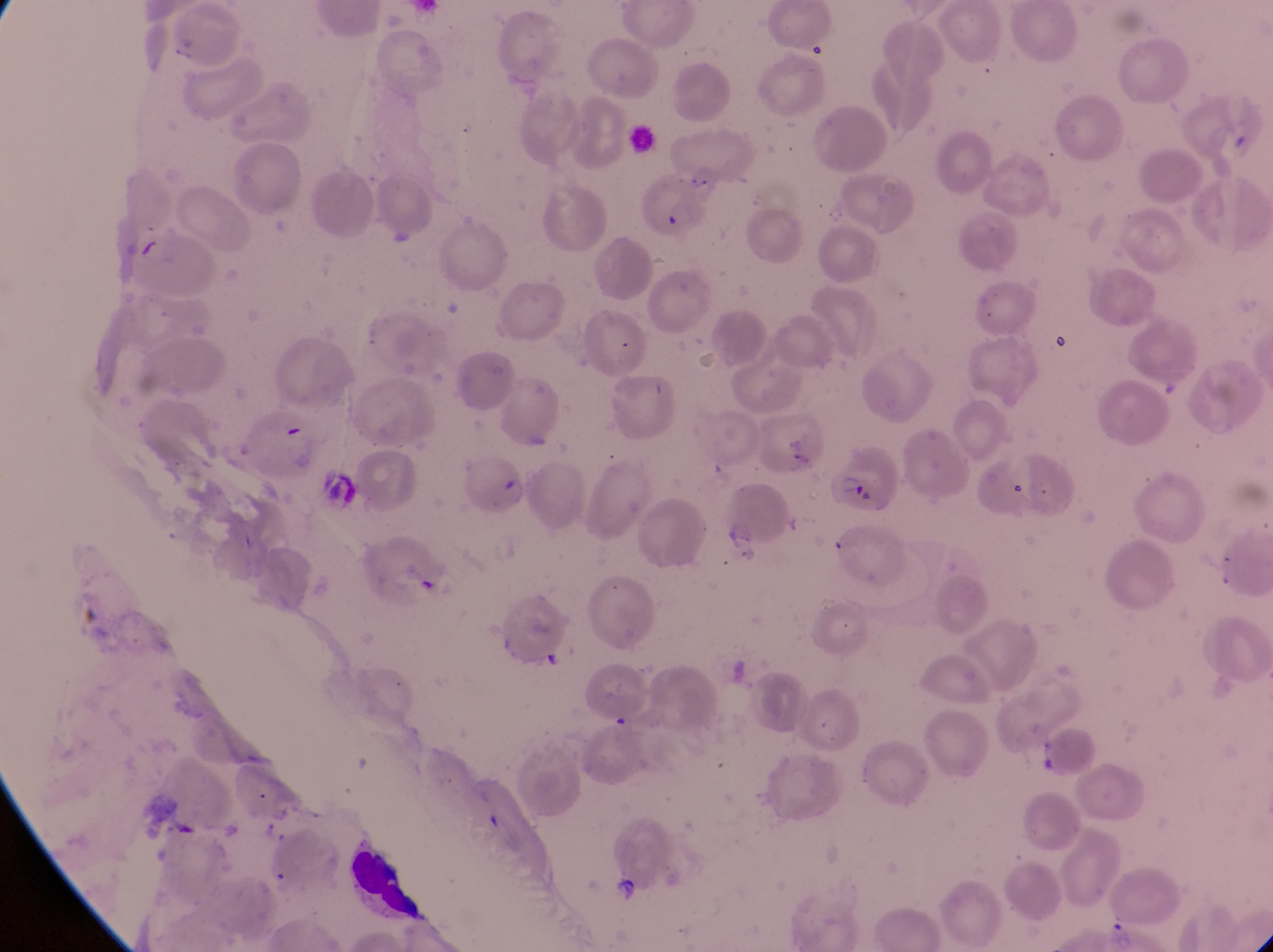
Approximate bounding boxes as (left, top, right, bottom) in pixels.
Summary:
  - Parasitised red blood cell locations: (627, 174, 707, 249), (754, 410, 823, 487), (452, 444, 529, 522), (834, 450, 908, 520)
  - Field of view: single
  - Preparation: thin blood smear
  - Country: Uganda
  - Capture: smartphone photograph through the eyepiece of an Olympus CX-23 microscope
  - Image size: 1273×952 pixels
  - Magnification: 1000x